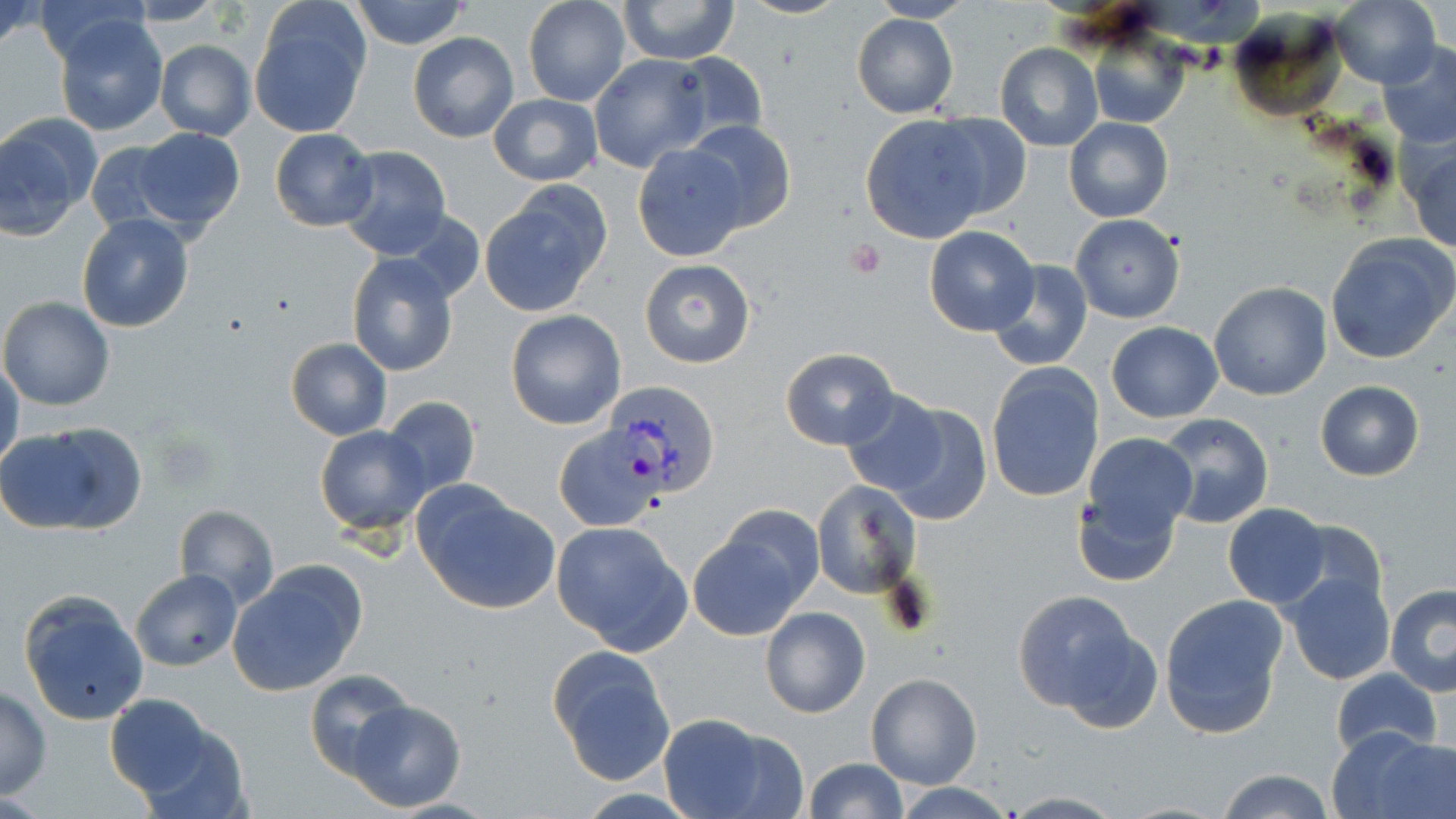
slide-level diagnosis = Plasmodium vivax
stain = May-Grünwald-Giemsa
Plasmodium vivax-infected red blood cell locations = approximate bounding boxes as named x1/y1/x2/y2 corners in pixels: (x1=606, y1=378, x2=721, y2=496)
magnification = 1000x
modality = optical microscopy
preparation = thin blood film
platelet locations = approximate bounding boxes as named x1/y1/x2/y2 corners in pixels: (x1=846, y1=239, x2=887, y2=278)
uninfected red blood cell locations = approximate bounding boxes as named x1/y1/x2/y2 corners in pixels: (x1=0, y1=0, x2=44, y2=55), (x1=349, y1=0, x2=471, y2=50), (x1=522, y1=0, x2=632, y2=106), (x1=737, y1=0, x2=849, y2=20), (x1=869, y1=0, x2=972, y2=24), (x1=1330, y1=0, x2=1440, y2=88), (x1=619, y1=1, x2=738, y2=65), (x1=119, y1=2, x2=225, y2=27), (x1=249, y1=2, x2=372, y2=138), (x1=53, y1=13, x2=169, y2=137), (x1=852, y1=13, x2=960, y2=118), (x1=1087, y1=29, x2=1189, y2=130), (x1=409, y1=32, x2=518, y2=142), (x1=154, y1=39, x2=255, y2=141), (x1=1377, y1=40, x2=1456, y2=148), (x1=994, y1=43, x2=1104, y2=152), (x1=670, y1=52, x2=769, y2=145), (x1=589, y1=54, x2=709, y2=172), (x1=488, y1=94, x2=601, y2=186), (x1=925, y1=113, x2=1033, y2=221), (x1=860, y1=115, x2=993, y2=244), (x1=1064, y1=117, x2=1174, y2=222), (x1=0, y1=118, x2=93, y2=237), (x1=680, y1=120, x2=796, y2=232), (x1=132, y1=128, x2=246, y2=233), (x1=269, y1=128, x2=376, y2=231), (x1=1403, y1=137, x2=1456, y2=254), (x1=83, y1=140, x2=183, y2=237), (x1=631, y1=142, x2=747, y2=262), (x1=335, y1=146, x2=452, y2=262), (x1=481, y1=186, x2=612, y2=315), (x1=395, y1=207, x2=487, y2=306), (x1=77, y1=213, x2=194, y2=333), (x1=1070, y1=213, x2=1185, y2=322), (x1=924, y1=225, x2=1039, y2=337), (x1=1325, y1=233, x2=1456, y2=365), (x1=346, y1=252, x2=458, y2=377), (x1=639, y1=258, x2=756, y2=367), (x1=988, y1=259, x2=1094, y2=372), (x1=1209, y1=281, x2=1332, y2=401), (x1=0, y1=296, x2=115, y2=412), (x1=505, y1=310, x2=626, y2=430), (x1=1104, y1=321, x2=1224, y2=422), (x1=285, y1=338, x2=392, y2=440), (x1=781, y1=347, x2=900, y2=451), (x1=0, y1=360, x2=23, y2=475), (x1=985, y1=363, x2=1105, y2=503), (x1=1315, y1=380, x2=1424, y2=481), (x1=838, y1=390, x2=952, y2=498), (x1=382, y1=398, x2=480, y2=499), (x1=880, y1=403, x2=991, y2=527), (x1=1153, y1=414, x2=1273, y2=530), (x1=4, y1=421, x2=148, y2=536), (x1=314, y1=425, x2=431, y2=533), (x1=555, y1=426, x2=668, y2=531), (x1=1084, y1=432, x2=1197, y2=537), (x1=810, y1=480, x2=922, y2=598), (x1=412, y1=481, x2=561, y2=615), (x1=1075, y1=492, x2=1180, y2=587), (x1=1223, y1=503, x2=1330, y2=607), (x1=718, y1=504, x2=826, y2=609), (x1=173, y1=505, x2=280, y2=607), (x1=551, y1=520, x2=692, y2=655), (x1=1280, y1=521, x2=1388, y2=619), (x1=687, y1=527, x2=812, y2=641), (x1=228, y1=562, x2=369, y2=695), (x1=132, y1=569, x2=241, y2=670), (x1=1283, y1=569, x2=1397, y2=687), (x1=1385, y1=581, x2=1456, y2=695), (x1=17, y1=590, x2=152, y2=727), (x1=1011, y1=590, x2=1149, y2=718), (x1=1159, y1=593, x2=1289, y2=739), (x1=760, y1=607, x2=870, y2=718), (x1=547, y1=645, x2=677, y2=785), (x1=303, y1=668, x2=416, y2=779), (x1=1331, y1=669, x2=1443, y2=758), (x1=866, y1=673, x2=982, y2=790), (x1=0, y1=687, x2=51, y2=797), (x1=104, y1=694, x2=219, y2=800), (x1=345, y1=700, x2=467, y2=810), (x1=656, y1=711, x2=797, y2=819), (x1=131, y1=717, x2=250, y2=818), (x1=1330, y1=724, x2=1454, y2=819), (x1=802, y1=757, x2=907, y2=819), (x1=1216, y1=767, x2=1335, y2=819), (x1=895, y1=783, x2=1015, y2=817), (x1=999, y1=792, x2=1126, y2=817)
field of view = single
image size = 1456×819 pixels